State which parasite is depicted.
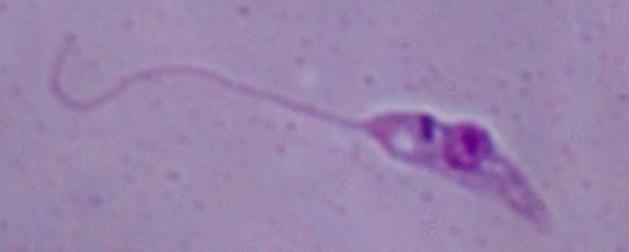

Leishmania.

Micrograph. 1000x magnification.